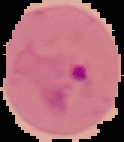
Summary:
  - Image type: segmented cell region with the area outside set to black
  - Malaria status: parasitized
  - Image size: 124×142 pixels
  - Preparation: thin blood film